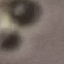

malaria_status: uninfected
stain: Giemsa
capture: smartphone through the microscope eyepiece
image_type: automatically extracted cell patch, resized to 64 × 64 pixels
preparation: thin smear